Assess this cell for malaria.
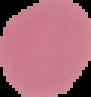
Uninfected.

From a thin blood film. Image is 91×97 pixels. Cell region segmented out of the field of view; the surrounding area is masked to black.